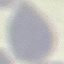

{
  "malaria_status": "uninfected",
  "capture": "smartphone through the microscope eyepiece",
  "stain": "Giemsa",
  "preparation": "thin smear",
  "image_type": "cell patch, automatically extracted from a larger field of view and resized to 64 × 64 pixels"
}